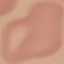
Summary:
  - Malaria status: uninfected
  - Capture: smartphone through the microscope eyepiece
  - Stain: Giemsa
  - Image type: automatically extracted cell patch, resized to 64 × 64 pixels
  - Preparation: thin blood film